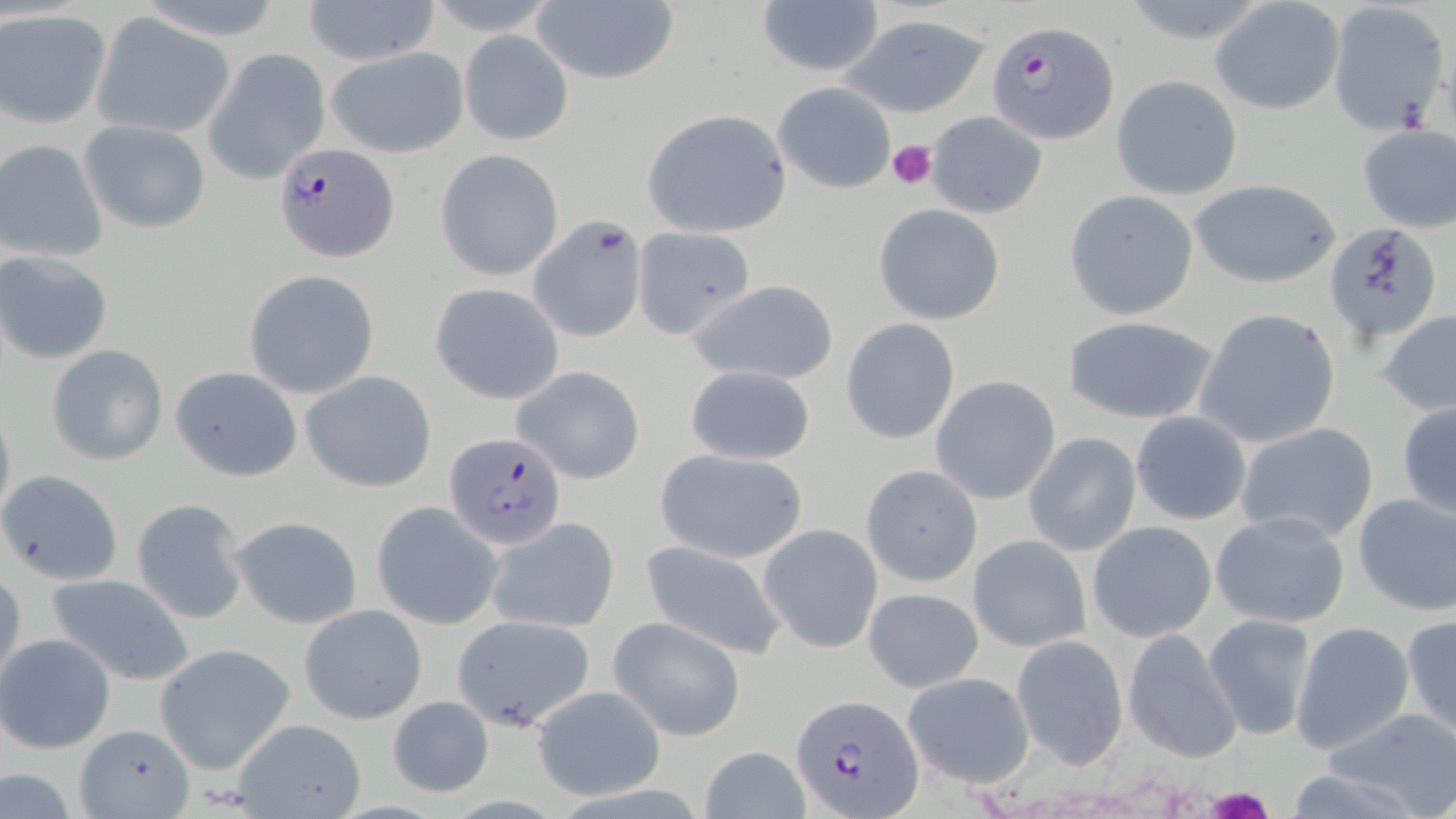
Approximate bounding boxes as named x1/y1/x2/y2 corners in pixels. Plasmodium falciparum-infected red blood cell locations: (x1=986, y1=19, x2=1119, y2=143), (x1=274, y1=143, x2=399, y2=261), (x1=445, y1=433, x2=566, y2=547), (x1=793, y1=693, x2=924, y2=817). Uninfected red blood cell locations: (x1=302, y1=0, x2=440, y2=65), (x1=531, y1=1, x2=679, y2=86), (x1=1209, y1=1, x2=1345, y2=116), (x1=756, y1=2, x2=885, y2=78), (x1=1325, y1=2, x2=1451, y2=134), (x1=0, y1=10, x2=111, y2=127), (x1=91, y1=14, x2=236, y2=138), (x1=842, y1=14, x2=991, y2=116), (x1=459, y1=30, x2=573, y2=145), (x1=325, y1=46, x2=468, y2=157), (x1=204, y1=48, x2=332, y2=183), (x1=1111, y1=76, x2=1242, y2=199), (x1=773, y1=82, x2=895, y2=195), (x1=641, y1=109, x2=791, y2=238), (x1=925, y1=110, x2=1049, y2=219), (x1=79, y1=120, x2=211, y2=235), (x1=1355, y1=123, x2=1455, y2=232), (x1=0, y1=140, x2=108, y2=262), (x1=436, y1=148, x2=565, y2=281), (x1=1189, y1=179, x2=1342, y2=288), (x1=1063, y1=189, x2=1201, y2=320), (x1=873, y1=202, x2=1006, y2=325), (x1=527, y1=215, x2=649, y2=342), (x1=1323, y1=222, x2=1443, y2=344), (x1=631, y1=228, x2=755, y2=340), (x1=1, y1=252, x2=113, y2=364), (x1=244, y1=270, x2=379, y2=398), (x1=684, y1=279, x2=839, y2=386), (x1=430, y1=282, x2=565, y2=404), (x1=1192, y1=307, x2=1341, y2=449), (x1=1377, y1=309, x2=1456, y2=416), (x1=1062, y1=315, x2=1220, y2=424), (x1=842, y1=318, x2=960, y2=443), (x1=46, y1=343, x2=168, y2=465), (x1=171, y1=365, x2=302, y2=482), (x1=512, y1=365, x2=645, y2=484), (x1=684, y1=365, x2=816, y2=465), (x1=301, y1=370, x2=437, y2=492), (x1=930, y1=376, x2=1060, y2=505), (x1=0, y1=397, x2=16, y2=530), (x1=1395, y1=400, x2=1456, y2=523), (x1=1132, y1=410, x2=1253, y2=526), (x1=1234, y1=422, x2=1380, y2=545), (x1=1024, y1=433, x2=1141, y2=555), (x1=655, y1=448, x2=808, y2=564), (x1=861, y1=464, x2=983, y2=587), (x1=1, y1=468, x2=123, y2=585), (x1=1352, y1=491, x2=1456, y2=615), (x1=131, y1=498, x2=249, y2=622), (x1=372, y1=500, x2=503, y2=630), (x1=1211, y1=511, x2=1351, y2=628), (x1=231, y1=516, x2=362, y2=629), (x1=487, y1=516, x2=620, y2=634), (x1=1086, y1=520, x2=1217, y2=642), (x1=759, y1=524, x2=882, y2=652), (x1=968, y1=535, x2=1090, y2=652), (x1=640, y1=541, x2=789, y2=659), (x1=1, y1=567, x2=25, y2=687), (x1=44, y1=572, x2=195, y2=684), (x1=863, y1=587, x2=984, y2=692), (x1=300, y1=604, x2=426, y2=723), (x1=1202, y1=614, x2=1317, y2=740), (x1=1402, y1=614, x2=1456, y2=741), (x1=451, y1=615, x2=598, y2=731), (x1=610, y1=616, x2=746, y2=741), (x1=1290, y1=619, x2=1416, y2=756), (x1=1121, y1=629, x2=1244, y2=761), (x1=1, y1=633, x2=116, y2=753), (x1=1012, y1=636, x2=1129, y2=767), (x1=155, y1=644, x2=294, y2=774), (x1=901, y1=672, x2=1034, y2=788), (x1=530, y1=684, x2=667, y2=800), (x1=388, y1=694, x2=495, y2=798), (x1=1322, y1=707, x2=1456, y2=817), (x1=233, y1=718, x2=368, y2=819), (x1=77, y1=723, x2=191, y2=817), (x1=700, y1=744, x2=809, y2=819), (x1=1283, y1=763, x2=1439, y2=819). Platelet locations: (x1=887, y1=138, x2=937, y2=190), (x1=1205, y1=786, x2=1274, y2=819). Slide-level diagnosis: Plasmodium falciparum. May-Grünwald-Giemsa-stained preparation. Thin blood smear. Image is 1456×819 pixels. 1000x magnification. Optical microscopy. One field of a larger specimen.